Assess the morphology of the erythrocytes.
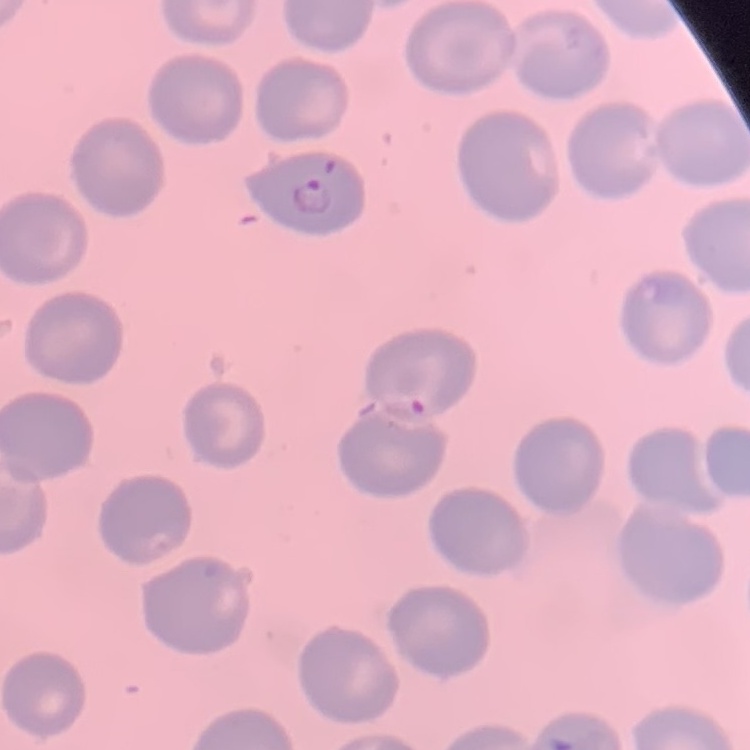
No rouleaux formation.

stain = Field's or Giemsa
preparation = thin blood film
image type = square crop of a larger photomicrograph